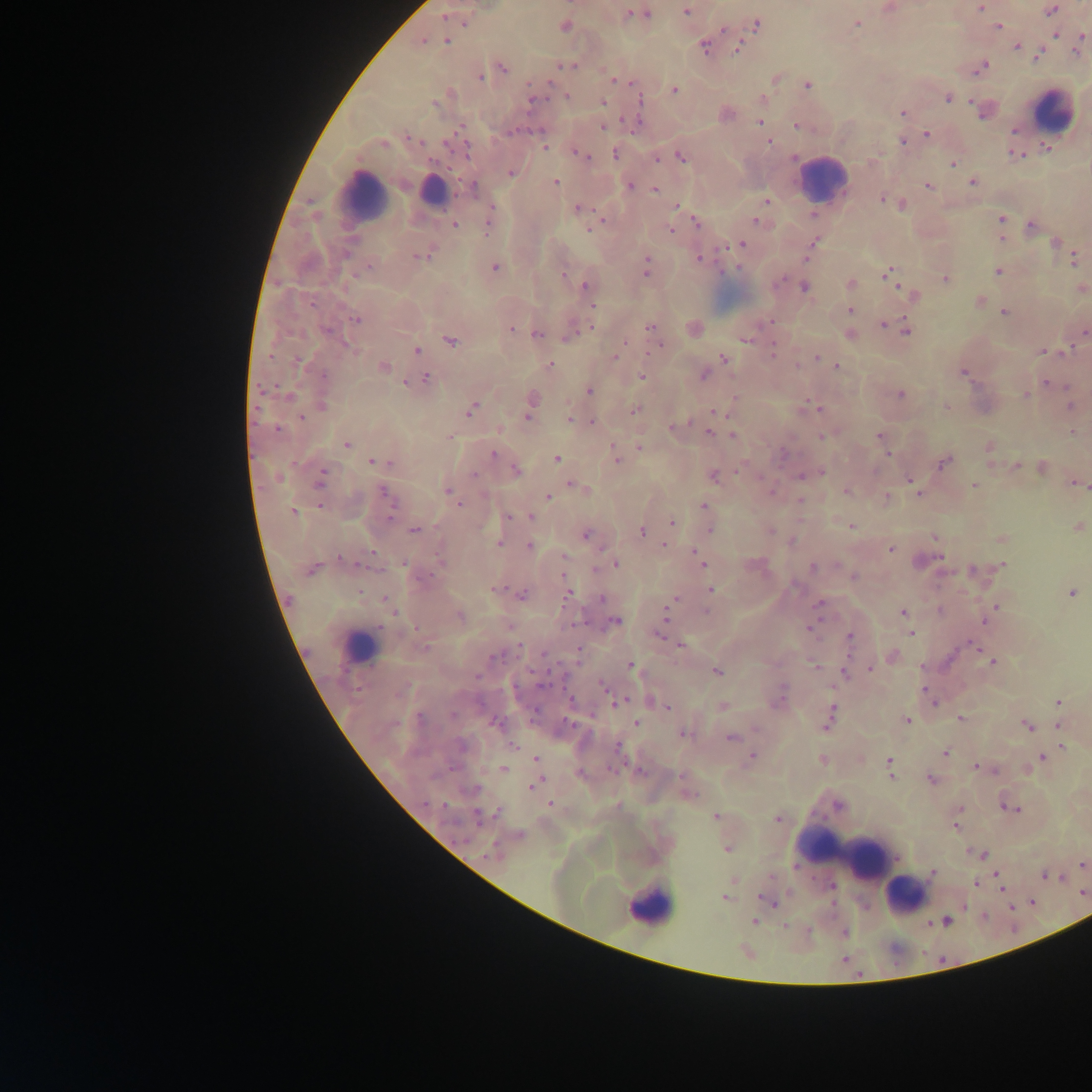
field of view = single
leukocyte locations = approximate centers as [x, y] in pixels: [1051, 111], [822, 180], [433, 191], [362, 197], [358, 646], [849, 857], [905, 896], [649, 906]
image size = 1092×1092 pixels
malaria parasite locations = approximate centers as [x, y] in pixels: [888, 8], [981, 8], [1050, 10], [686, 11], [643, 14], [445, 18], [455, 19], [463, 20], [856, 23], [757, 24], [565, 26], [998, 26], [723, 29], [1055, 33], [421, 41], [447, 41], [1078, 44], [704, 46], [1017, 46], [737, 47], [1037, 54], [566, 65], [502, 67], [980, 67], [479, 77], [775, 77], [613, 79], [807, 85], [673, 89], [947, 96], [567, 97], [533, 99], [640, 99], [602, 101], [761, 101], [984, 110], [903, 113], [759, 122], [797, 125], [603, 126], [927, 133], [769, 141], [903, 141], [1046, 145], [544, 147], [578, 152], [616, 153], [1015, 154], [583, 155], [680, 156], [656, 157], [952, 164], [510, 172], [972, 181], [554, 182], [629, 185], [928, 185], [473, 188], [655, 189], [885, 199], [766, 200], [893, 201], [901, 203], [676, 205], [578, 208], [491, 211], [1001, 219], [489, 220], [696, 221], [757, 221], [596, 223], [454, 224], [1031, 226], [670, 230], [1002, 236], [1056, 242], [812, 243], [741, 244], [421, 255], [699, 258], [1074, 258], [494, 268], [646, 268], [889, 272], [998, 272], [563, 274], [945, 278], [850, 284], [586, 285], [804, 286], [1081, 288], [914, 295], [979, 301], [592, 304], [848, 309], [1004, 312], [355, 319], [770, 321], [849, 322], [883, 323], [650, 327], [511, 328], [693, 328], [906, 329], [571, 332], [1084, 332], [537, 333], [849, 333], [449, 339], [746, 339], [773, 348], [651, 349], [417, 351], [1043, 351], [616, 357], [723, 357], [816, 357], [550, 365], [382, 366], [835, 366], [963, 371], [703, 373], [642, 376], [425, 379], [1046, 382], [588, 390], [900, 394], [1026, 394], [529, 402], [322, 405], [1070, 405], [946, 407], [818, 408], [471, 409], [634, 409], [715, 411], [302, 417], [569, 420], [591, 422], [675, 425], [708, 432], [1073, 432], [733, 435], [824, 436], [880, 436], [346, 444], [640, 445], [989, 448], [493, 454], [615, 457], [556, 458], [944, 461], [375, 462], [1016, 465], [1041, 467], [515, 470], [820, 471], [804, 474], [713, 475], [320, 478], [910, 479], [1075, 482], [576, 485], [974, 485], [584, 489], [846, 490], [771, 491], [450, 493], [918, 493], [386, 495], [548, 496], [886, 498], [800, 501], [703, 506], [294, 511], [508, 516], [530, 517], [672, 523], [850, 526], [1077, 526], [709, 528], [414, 530], [641, 530], [769, 530], [585, 534], [935, 537], [1002, 538], [792, 542], [498, 543], [665, 543], [529, 546], [890, 549], [695, 552], [938, 556], [702, 562], [615, 563], [405, 564], [1002, 565], [812, 567], [312, 568], [972, 570], [854, 576], [496, 589], [710, 589], [568, 591], [1072, 592], [521, 594], [675, 598], [386, 601], [818, 604], [995, 606], [668, 612], [902, 612], [992, 612], [458, 616], [985, 620], [614, 621], [664, 622], [907, 622], [811, 628], [911, 632], [660, 633], [849, 637], [681, 644], [973, 645], [892, 656], [992, 661], [630, 666], [815, 667], [870, 669], [716, 671], [845, 672], [603, 685], [650, 700], [778, 700], [933, 701], [1058, 701], [618, 702], [661, 703], [667, 706], [722, 706], [828, 717], [959, 718], [906, 721], [636, 723], [1026, 725], [1058, 725], [682, 732], [731, 737], [1061, 745], [944, 752], [751, 756], [1042, 757], [536, 759], [822, 759], [890, 762], [976, 766], [503, 769], [538, 772], [889, 774], [930, 779], [536, 783], [686, 792], [550, 804], [1005, 805], [1012, 808], [959, 810], [480, 816], [716, 817], [778, 819], [955, 825], [518, 836], [727, 848], [982, 854], [1082, 864], [933, 872], [997, 875], [1045, 875], [976, 883], [1001, 888], [725, 897], [770, 901], [754, 921], [942, 922], [783, 926], [746, 952]
preparation = thick blood film
country = Ghana
capture = mobile-phone photograph through a microscope